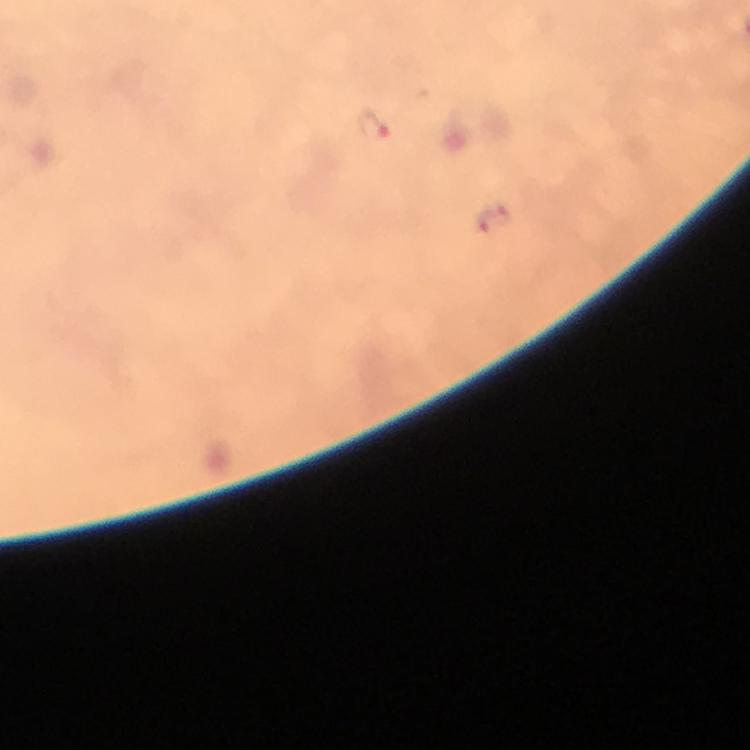
Approximate centers as [x, y] in pixels.
Summary:
  - Malaria parasite locations: [373, 125], [493, 220]
  - Cropped from: a single field of view
  - Immersion oil: applied
  - Magnification: 100x
  - Preparation: thick blood film
  - Stain: Giemsa
  - Capture: smartphone photograph through a microscope
  - Image size: 750×750 pixels
  - Context: from a malaria diagnostic workup